State the blood parasite species.
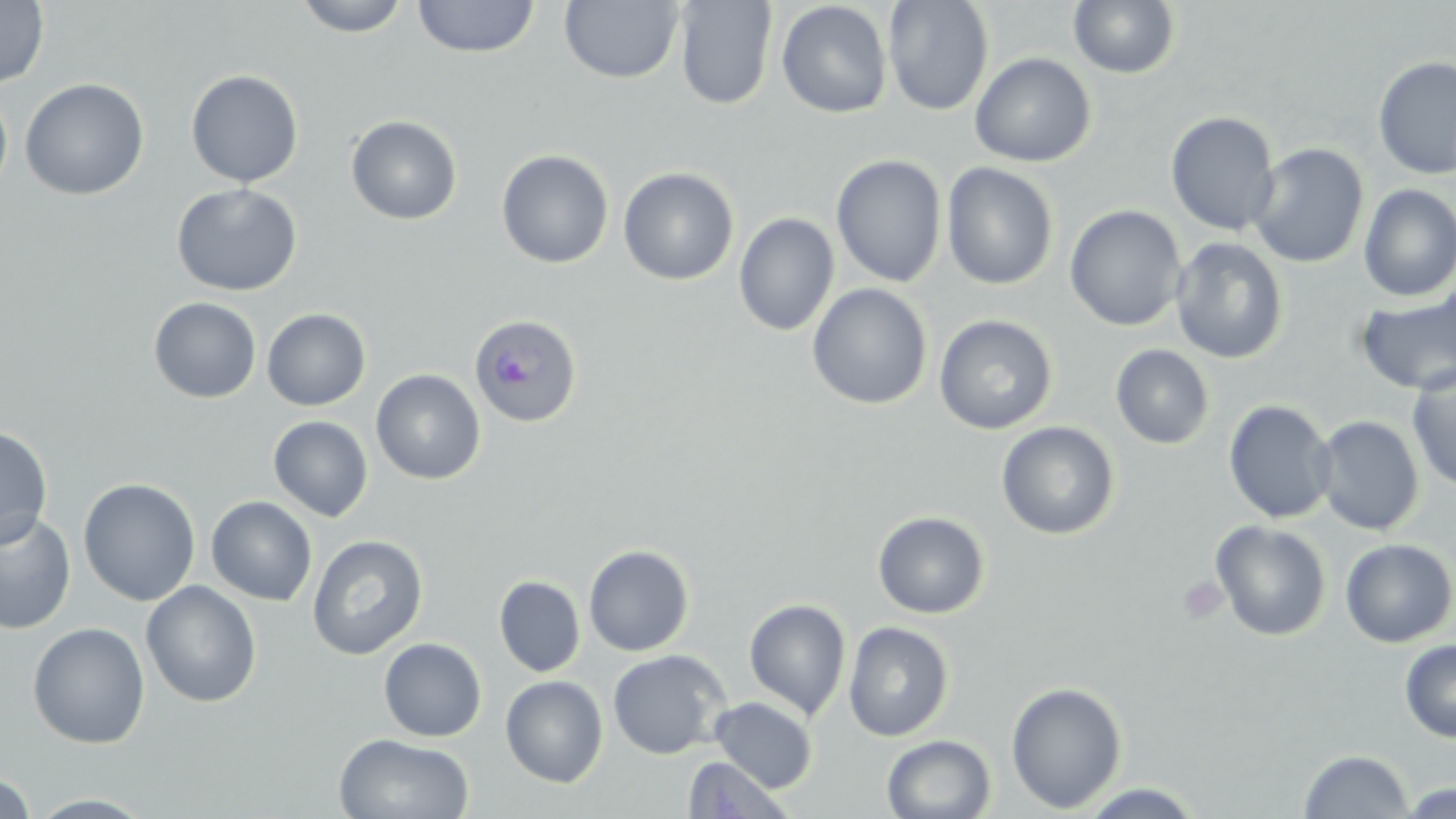

Plasmodium ovale.

Approximate bounding boxes as (x1, y1, x2, y2) in pixels. Platelet locations: (1176, 575, 1229, 625). Plasmodium ovale-infected red blood cell locations: (469, 313, 582, 428). Uninfected red blood cell locations: (0, 0, 49, 89), (293, 0, 412, 37), (413, 0, 540, 59), (559, 0, 684, 84), (882, 0, 994, 116), (1068, 0, 1181, 79), (674, 1, 777, 109), (776, 1, 894, 119), (969, 52, 1096, 167), (1372, 56, 1456, 180), (185, 69, 304, 188), (20, 77, 150, 201), (0, 83, 13, 199), (1165, 111, 1280, 237), (346, 115, 463, 225), (1248, 142, 1369, 269), (496, 149, 614, 269), (831, 154, 947, 288), (495, 160, 739, 274), (941, 162, 1059, 290), (618, 167, 739, 285), (171, 183, 302, 297), (1357, 184, 1456, 302), (1065, 204, 1187, 331), (733, 212, 839, 337), (1170, 237, 1288, 364), (807, 283, 932, 410), (1354, 287, 1456, 397), (148, 297, 261, 403), (261, 308, 371, 411), (934, 314, 1058, 434), (1110, 344, 1215, 450), (1405, 365, 1456, 492), (371, 369, 486, 485), (1223, 399, 1337, 524), (268, 415, 373, 522), (1313, 415, 1425, 536), (996, 421, 1120, 540), (0, 424, 53, 548), (78, 478, 201, 606), (206, 496, 317, 606), (0, 509, 76, 635), (872, 510, 991, 619), (1210, 519, 1331, 642), (306, 534, 428, 660), (1339, 538, 1456, 647), (583, 544, 695, 657), (494, 575, 585, 677), (141, 581, 262, 708), (744, 598, 851, 720), (843, 621, 954, 742), (28, 622, 150, 749), (379, 637, 487, 742), (1399, 638, 1456, 743), (607, 649, 731, 759), (500, 675, 608, 788), (1005, 681, 1128, 813), (709, 697, 818, 792), (334, 733, 474, 819), (881, 734, 996, 818), (1298, 749, 1414, 818), (681, 755, 793, 818), (0, 773, 37, 818), (1075, 783, 1207, 818), (1400, 784, 1454, 818), (26, 793, 155, 818). May-Grünwald-Giemsa stain. Single field of view. Image is 1456×819 pixels. Thin blood smear. Light microscopy. 1000x magnification.